Report the malaria status of this cell.
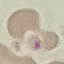

Uninfected.

Summary:
  - Preparation: thin blood film
  - Stain: Giemsa
  - Capture: smartphone through the microscope eyepiece
  - Image type: automatically extracted cell patch, resized to 64 × 64 pixels